State which cell type is depicted.
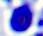

This is a leukocyte.

Summary:
  - Modality: micrograph
  - Magnification: 400x